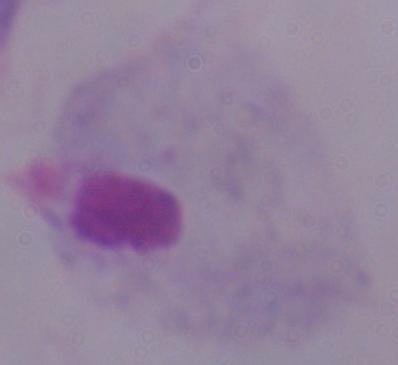
Summary:
  - Modality: micrograph
  - Identification: trichomonad
  - Magnification: 1000x